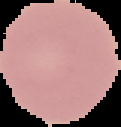 From a thin blood film. Result: no Plasmodium parasites seen. Image is 121×127 pixels. The area outside the segmented cell region is set to black.